Name the parasite shown.
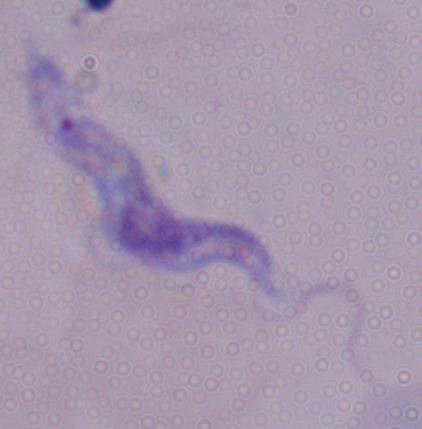
A trypanosome.

Captured at 1000x magnification. Photomicrograph.